Report the malaria status of this cell.
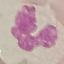
It is uninfected.

Thin smear of blood. Acquired by smartphone through the microscope eyepiece. Cell patch, automatically extracted from a larger field of view and resized to 64 × 64 pixels. Giemsa stain.